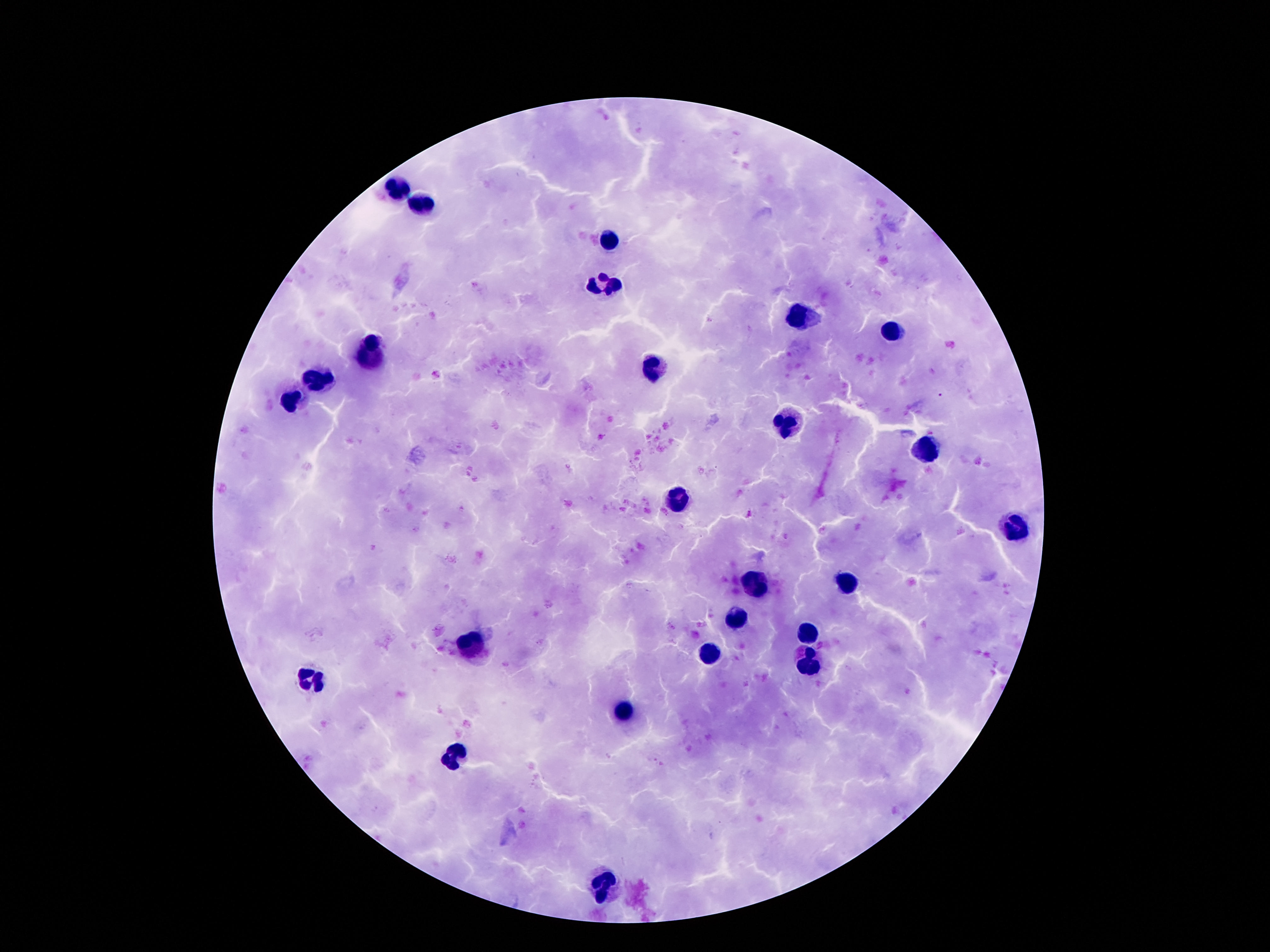

Approximate centers as {x, y} in pixels.
Summary:
  - Leukocyte locations: {395, 190}, {421, 204}, {612, 243}, {600, 285}, {800, 317}, {892, 331}, {370, 348}, {651, 368}, {317, 379}, {294, 400}, {786, 422}, {927, 452}, {682, 502}, {1017, 528}, {757, 581}, {847, 583}, {737, 619}, {807, 635}, {471, 642}, {708, 652}, {809, 662}, {313, 679}, {624, 711}, {456, 760}, {602, 886}
  - Field of view: one from this slide
  - Magnification: 100x
  - Image size: 1270×952 pixels
  - Stain: Giemsa
  - Patient malaria status: negative
  - Capture: smartphone camera through the microscope eyepiece
  - Preparation: thick peripheral-blood smear